Comment on the morphology of the erythrocytes.
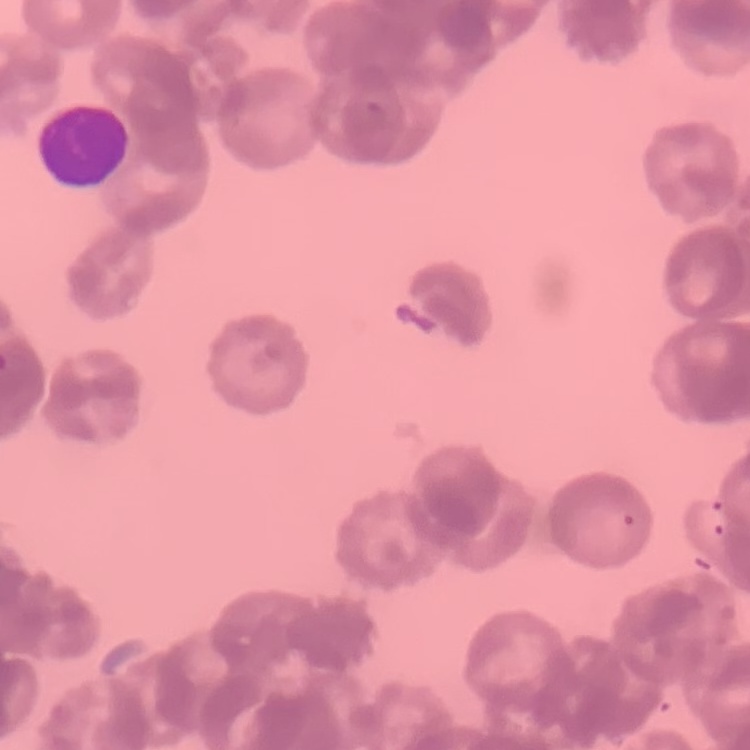

Rouleaux formation.

Thin peripheral smear. Field's or Giemsa stain. One tile cut from a larger photomicrograph.